Name the parasite shown.
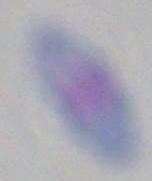

Toxoplasma gondii.

modality = photomicrograph
magnification = 1000x